Identify the blood parasite species.
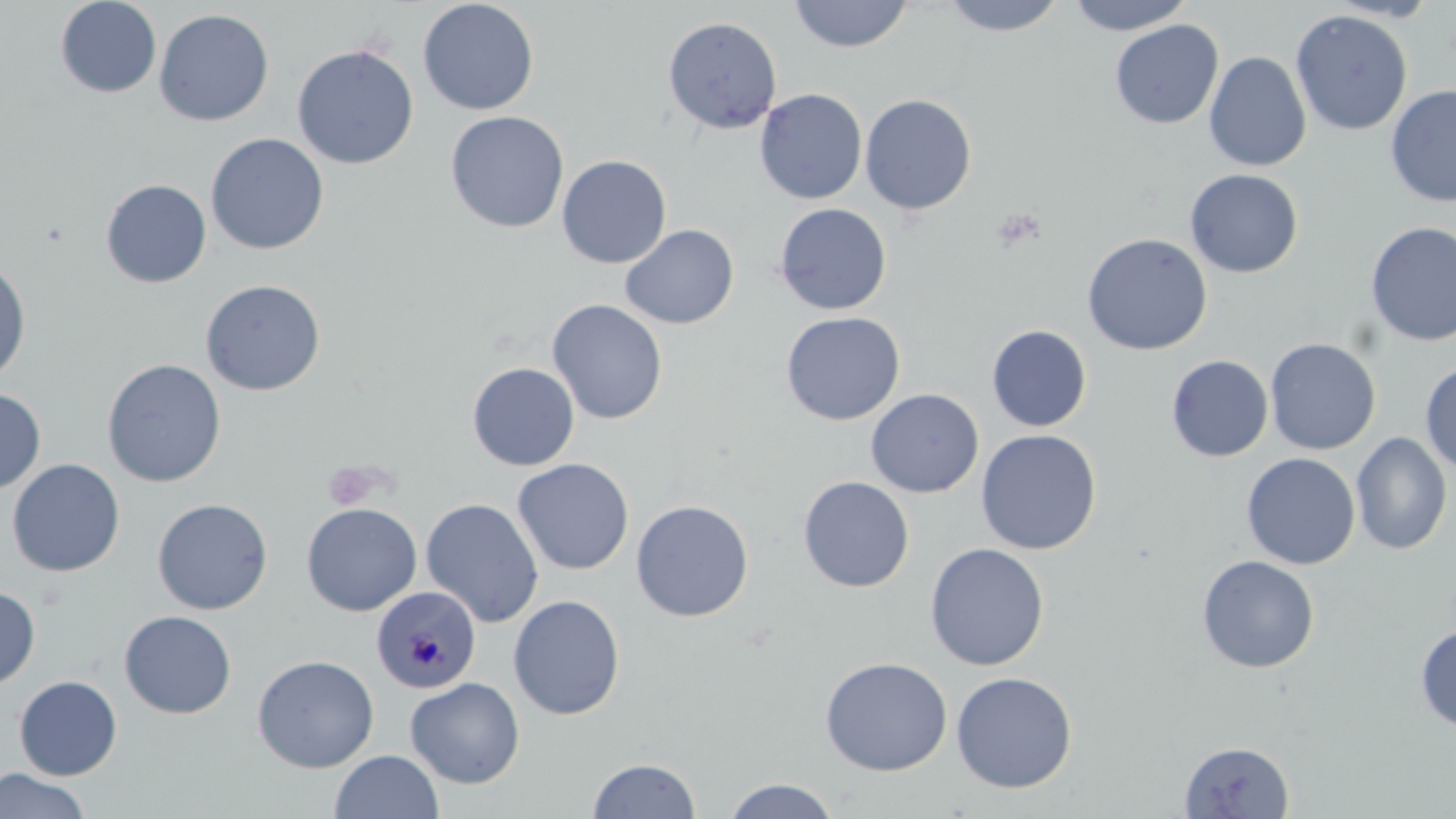
Plasmodium malariae.

preparation: thin blood smear
platelet_locations: 'approximate bounding boxes as [x1, y1, x2, y2] in pixels: [323, 461, 378, 511]'
uninfected_red_blood_cell_locations: 'approximate bounding boxes as [x1, y1, x2, y2] in pixels: [55, 0, 161, 98], [418, 0, 539, 115], [787, 0, 914, 53], [938, 0, 1068, 36], [1065, 0, 1195, 35], [153, 8, 275, 127], [1290, 9, 1413, 136], [662, 16, 783, 134], [1109, 19, 1224, 129], [291, 43, 419, 170], [1204, 51, 1312, 172], [1384, 84, 1456, 207], [754, 88, 868, 205], [859, 93, 977, 216], [445, 111, 569, 233], [205, 132, 330, 255], [556, 154, 672, 269], [1184, 168, 1303, 278], [100, 179, 212, 288], [774, 203, 892, 315], [1364, 221, 1456, 346], [620, 224, 738, 329], [1081, 232, 1213, 355], [0, 257, 32, 385], [200, 279, 326, 396], [546, 298, 668, 425], [779, 311, 906, 426], [986, 324, 1092, 432], [1264, 337, 1381, 455], [1166, 355, 1273, 462], [101, 358, 227, 488], [1419, 360, 1456, 474], [466, 362, 580, 470], [0, 387, 46, 494], [865, 388, 984, 498], [975, 428, 1102, 555], [1351, 432, 1452, 555], [1241, 452, 1360, 570], [511, 457, 634, 576], [7, 458, 125, 577], [798, 476, 915, 593], [152, 497, 273, 615], [420, 497, 544, 628], [630, 499, 754, 622], [301, 502, 422, 616], [924, 543, 1049, 671], [939, 545, 1057, 797], [1196, 554, 1320, 673], [0, 585, 40, 690], [508, 594, 626, 720], [119, 610, 237, 719], [1415, 624, 1456, 731], [251, 654, 379, 773], [819, 657, 953, 776], [950, 671, 1078, 793], [13, 675, 122, 780], [405, 676, 525, 788], [1179, 740, 1295, 818], [330, 749, 443, 818], [586, 757, 701, 818], [0, 768, 92, 819], [722, 777, 841, 819]'
modality: optical microscopy
stain: May-Grünwald-Giemsa
magnification: 1000x
plasmodium_malariae_infected_red_blood_cell_locations: 'approximate bounding boxes as [x1, y1, x2, y2] in pixels: [372, 588, 480, 697]'
image_size: 1456×819 pixels
field_of_view: one of a larger specimen